Report the malaria status of this cell.
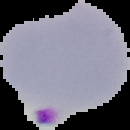

Parasitized.

preparation = thin blood film
image type = cell region segmented out of the field of view; surrounding area masked to black
image size = 130×130 pixels